Assess this cell for malaria.
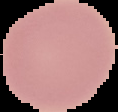

Uninfected.

From a thin blood smear. Image is 118×112 pixels. Segmented cell region on a black background.